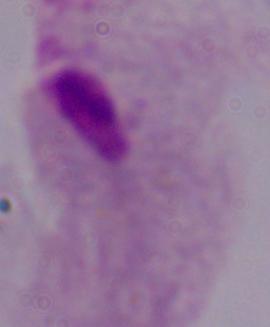
Summary:
  - Modality: photomicrograph
  - Identification: trichomonad
  - Magnification: 1000x